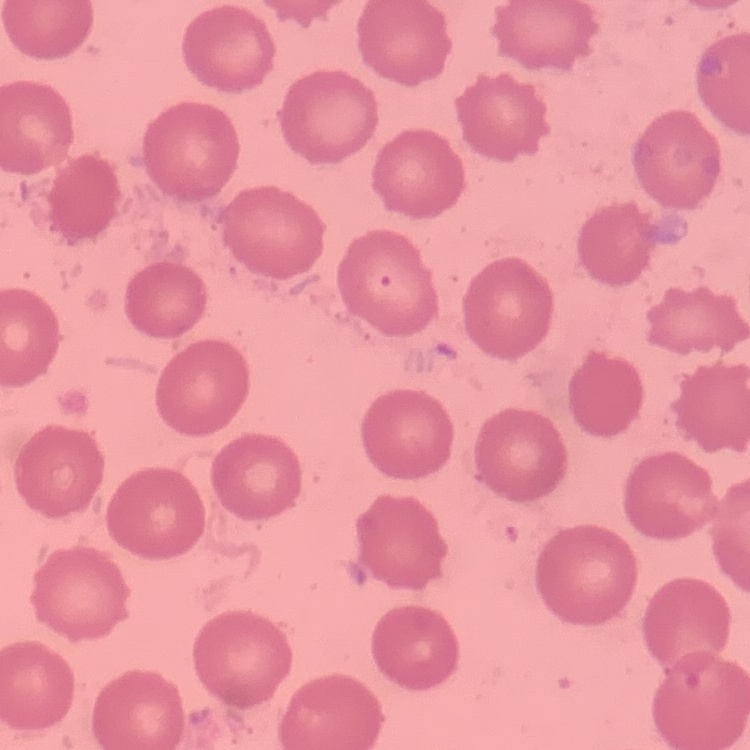
red_blood_cell_morphology: no rouleaux formation
stain: Field's or Giemsa
image_type: square crop of a larger photomicrograph
preparation: thin peripheral smear